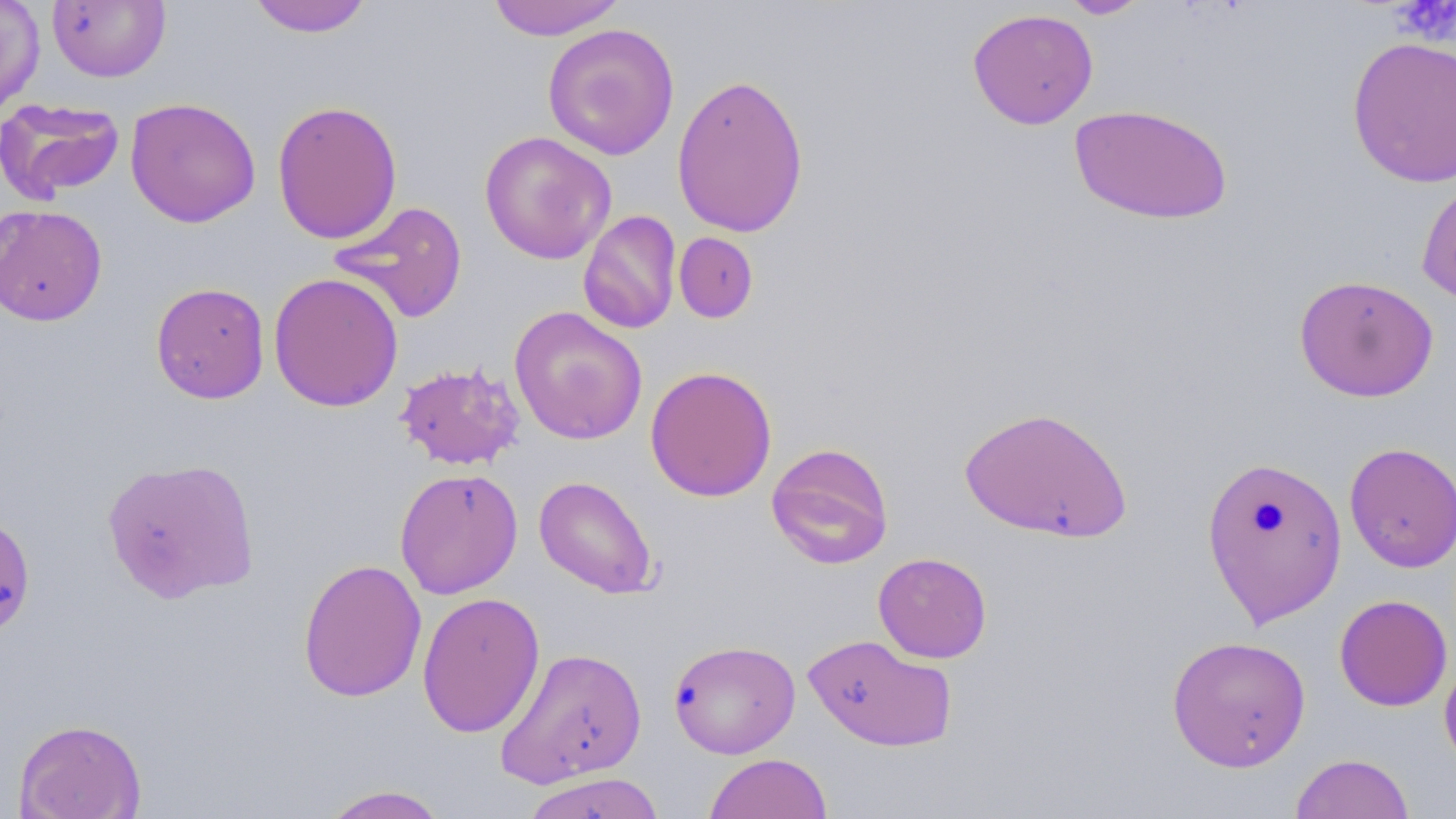

Summary:
  - Coordinate format: approximate bounding boxes as named x1/y1/x2/y2 corners in pixels
  - Uninfected red blood cell locations: (x1=0, y1=0, x2=44, y2=119), (x1=247, y1=0, x2=373, y2=37), (x1=486, y1=0, x2=626, y2=40), (x1=1060, y1=0, x2=1150, y2=19), (x1=47, y1=1, x2=170, y2=83), (x1=967, y1=8, x2=1099, y2=130), (x1=542, y1=23, x2=680, y2=161), (x1=1346, y1=35, x2=1456, y2=189), (x1=671, y1=72, x2=809, y2=238), (x1=124, y1=97, x2=262, y2=228), (x1=0, y1=98, x2=125, y2=203), (x1=272, y1=99, x2=403, y2=245), (x1=1069, y1=104, x2=1234, y2=225), (x1=479, y1=130, x2=617, y2=264), (x1=1417, y1=177, x2=1456, y2=307), (x1=328, y1=200, x2=469, y2=325), (x1=0, y1=204, x2=108, y2=326), (x1=578, y1=210, x2=682, y2=335), (x1=674, y1=232, x2=758, y2=323), (x1=268, y1=272, x2=404, y2=412), (x1=1294, y1=274, x2=1439, y2=401), (x1=150, y1=282, x2=270, y2=404), (x1=509, y1=306, x2=648, y2=445), (x1=395, y1=361, x2=525, y2=471), (x1=645, y1=365, x2=777, y2=502), (x1=959, y1=406, x2=1133, y2=543), (x1=1343, y1=441, x2=1456, y2=573), (x1=766, y1=442, x2=895, y2=569), (x1=1201, y1=455, x2=1349, y2=628), (x1=101, y1=456, x2=259, y2=603), (x1=394, y1=467, x2=523, y2=599), (x1=533, y1=475, x2=659, y2=599), (x1=873, y1=552, x2=992, y2=663), (x1=297, y1=558, x2=427, y2=702), (x1=417, y1=591, x2=545, y2=738), (x1=1334, y1=594, x2=1452, y2=711), (x1=802, y1=633, x2=957, y2=752), (x1=1166, y1=635, x2=1312, y2=772), (x1=669, y1=639, x2=800, y2=759), (x1=496, y1=647, x2=648, y2=787), (x1=1439, y1=650, x2=1456, y2=775), (x1=14, y1=718, x2=146, y2=819), (x1=1290, y1=752, x2=1415, y2=818), (x1=704, y1=753, x2=833, y2=818), (x1=520, y1=771, x2=669, y2=819), (x1=319, y1=784, x2=450, y2=819)
  - Platelet locations: (x1=1392, y1=0, x2=1456, y2=42)
  - Slide-level diagnosis: negative for blood parasites
  - Modality: light microscopy
  - Field of view: one of a larger specimen
  - Magnification: 1000x
  - Image size: 1456×819 pixels
  - Preparation: thin blood smear
  - Stain: May-Grünwald-Giemsa